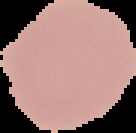
Summary:
  - Malaria status: uninfected
  - Image size: 136×133 pixels
  - Preparation: thin blood film
  - Image type: cell region segmented out of the field of view; surrounding area masked to black